Give the position of every Plasmodium parasite.
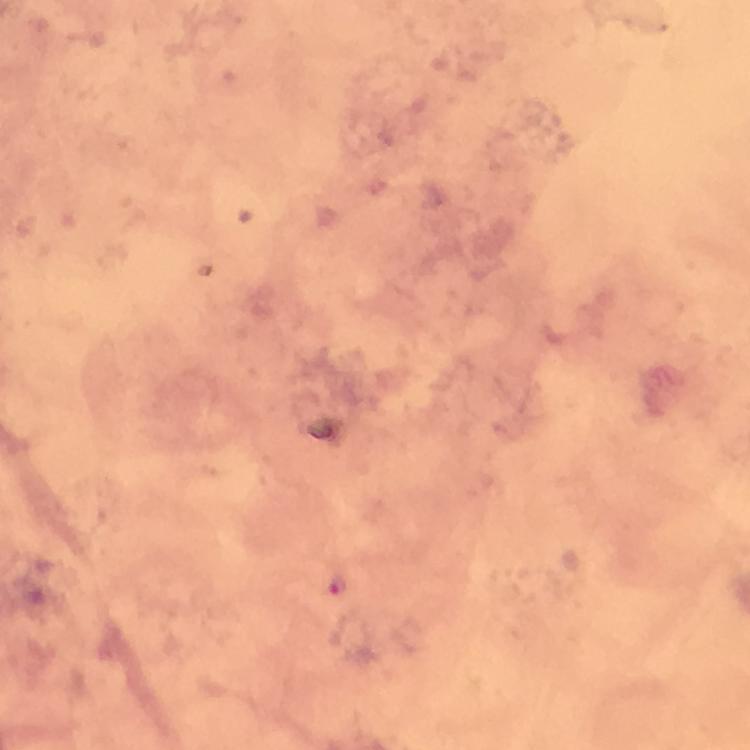
Approximate centers as {x, y} in pixels.
Plasmodium parasites: {339, 585}.

Thick smear. Photographed through the microscope with a smartphone camera. From a diagnostic examination for malaria. Giemsa stain. Immersion oil applied. Image is 750×750 pixels. At 100x magnification. Cropped region of a single field of view.